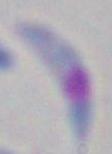

identification = Toxoplasma gondii
magnification = 1000x
modality = photomicrograph